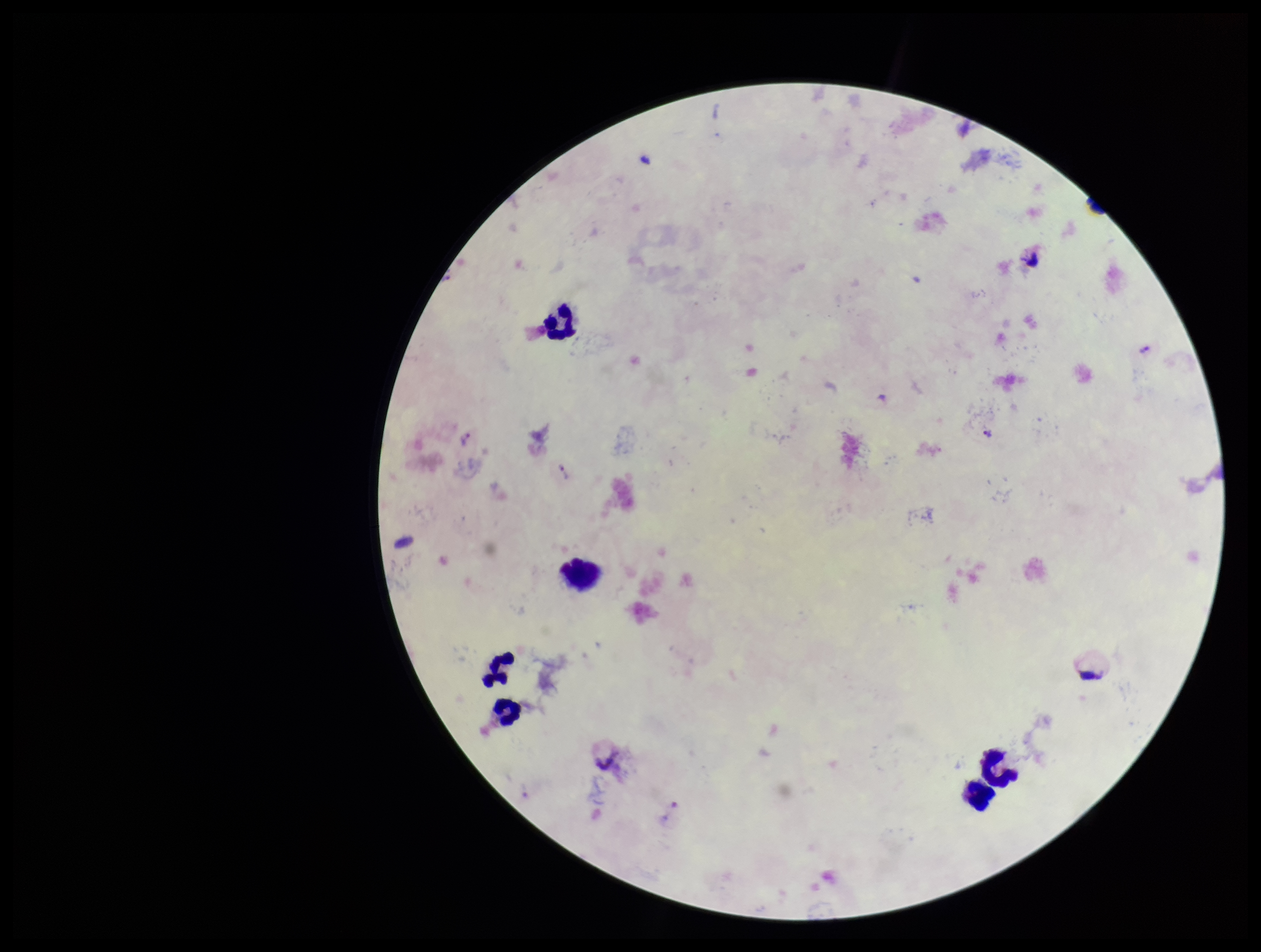
Summary:
  - Leukocyte count: 6
  - Species reported for this patient: Plasmodium vivax
  - Field of view: one from this slide
  - Stain: Giemsa
  - Image size: 1261×952 pixels
  - Plasmodium parasites: none identified
  - Patient malaria status: infected
  - Preparation: thick blood smear
  - Parasite count: 0
  - Capture: smartphone photograph through the microscope eyepiece